Point out each leukocyte.
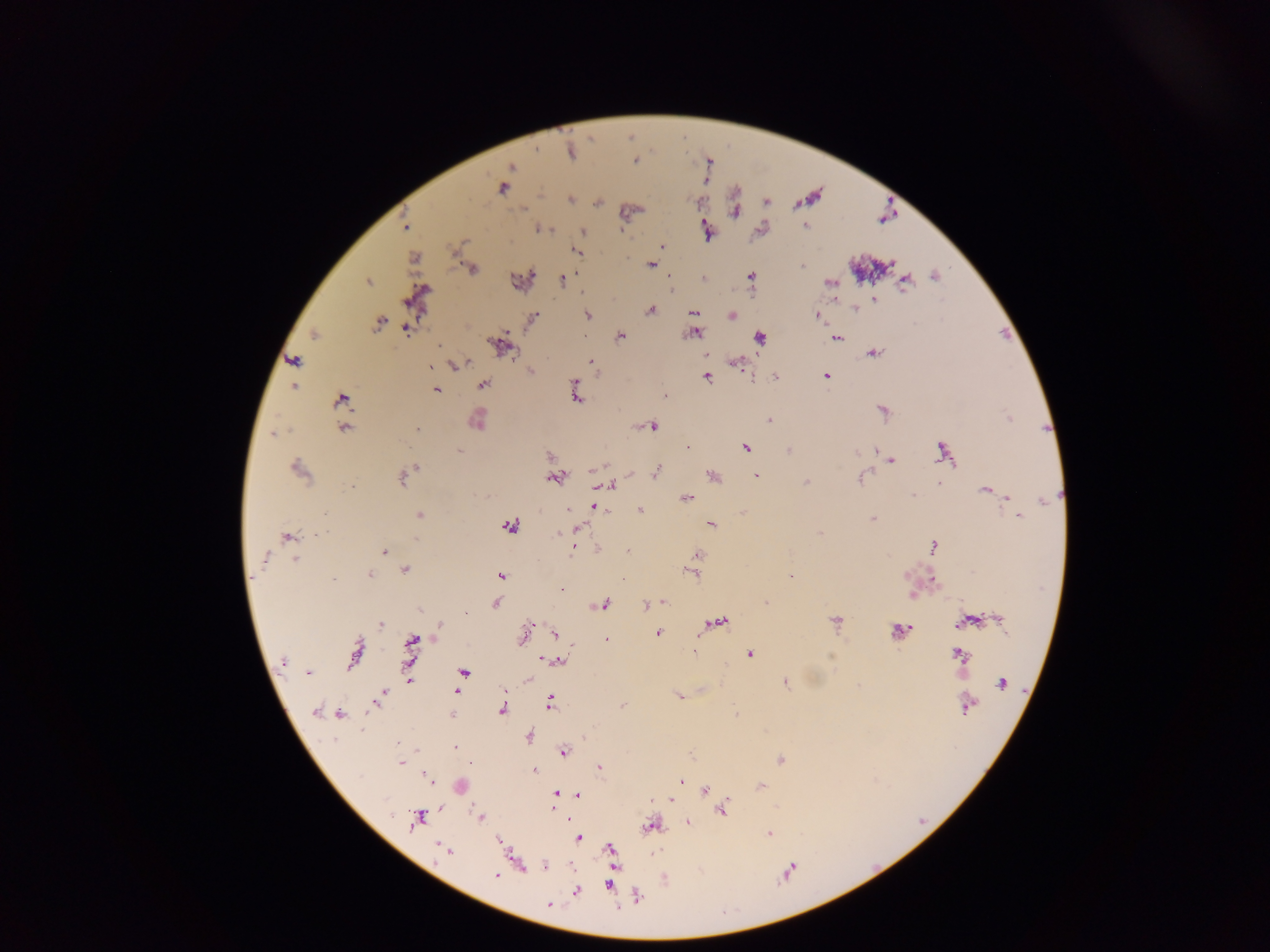

No leukocytes observed.

Approximate centers as [x, y] in pixels. Plasmodium parasite locations: [570, 151], [636, 160], [503, 186], [570, 200], [598, 201], [765, 202], [735, 210], [407, 226], [805, 226], [538, 228], [760, 228], [706, 231], [583, 232], [662, 247], [576, 252], [414, 259], [651, 264], [802, 265], [471, 268], [531, 274], [933, 275], [668, 276], [750, 276], [561, 279], [703, 279], [519, 280], [904, 280], [367, 281], [830, 282], [415, 296], [834, 299], [874, 299], [855, 307], [650, 310], [693, 313], [587, 314], [730, 315], [817, 315], [533, 317], [378, 321], [406, 328], [692, 332], [314, 334], [619, 336], [760, 337], [837, 338], [499, 345], [872, 352], [705, 353], [293, 361], [591, 361], [734, 362], [454, 365], [529, 371], [706, 376], [749, 376], [774, 376], [826, 376], [482, 384], [294, 385], [575, 385], [435, 390], [575, 393], [663, 395], [340, 399], [883, 411], [1009, 418], [476, 419], [770, 420], [651, 425], [344, 427], [417, 429], [274, 434], [687, 447], [745, 447], [875, 449], [459, 450], [788, 450], [943, 452], [550, 457], [890, 460], [298, 469], [409, 469], [655, 472], [712, 475], [755, 475], [404, 476], [554, 477], [861, 477], [806, 482], [940, 483], [605, 485], [352, 486], [985, 489], [992, 492], [913, 496], [1006, 497], [686, 498], [593, 506], [568, 509], [639, 510], [743, 512], [419, 514], [1019, 515], [873, 518], [710, 524], [508, 526], [575, 529], [820, 534], [287, 537], [574, 545], [933, 547], [599, 549], [383, 550], [628, 550], [696, 556], [263, 558], [296, 559], [405, 569], [692, 572], [369, 574], [501, 576], [791, 576], [561, 590], [911, 595], [663, 601], [496, 602], [766, 602], [601, 604], [653, 604], [647, 606], [465, 613], [996, 619], [835, 620], [965, 622], [439, 623], [716, 623], [380, 624], [897, 631], [555, 632], [657, 633], [522, 636], [606, 640], [410, 643], [693, 651], [355, 653], [749, 653], [409, 654], [958, 655], [283, 660], [555, 660], [411, 670], [464, 671], [307, 673], [409, 678], [527, 678], [784, 682], [1002, 683], [456, 692], [382, 694], [678, 695], [378, 700], [550, 701], [966, 704], [623, 705], [500, 710], [316, 712], [339, 713], [323, 714], [736, 714], [451, 715], [528, 735], [455, 748], [563, 751], [690, 753], [780, 759], [401, 763], [470, 764], [600, 767], [535, 771], [427, 776], [679, 781], [460, 786], [761, 787], [704, 791], [555, 793], [578, 795], [652, 800], [671, 800], [552, 806], [722, 809], [480, 817], [418, 818], [567, 819], [687, 822], [649, 826], [769, 834], [577, 838], [444, 850], [610, 850], [515, 861], [544, 865], [495, 876], [609, 884], [576, 890], [549, 904]. Sample from Ghana. Thick blood smear. Single field of view. Image is 1270×952 pixels. Photographed through a microscope with a mobile-phone camera.